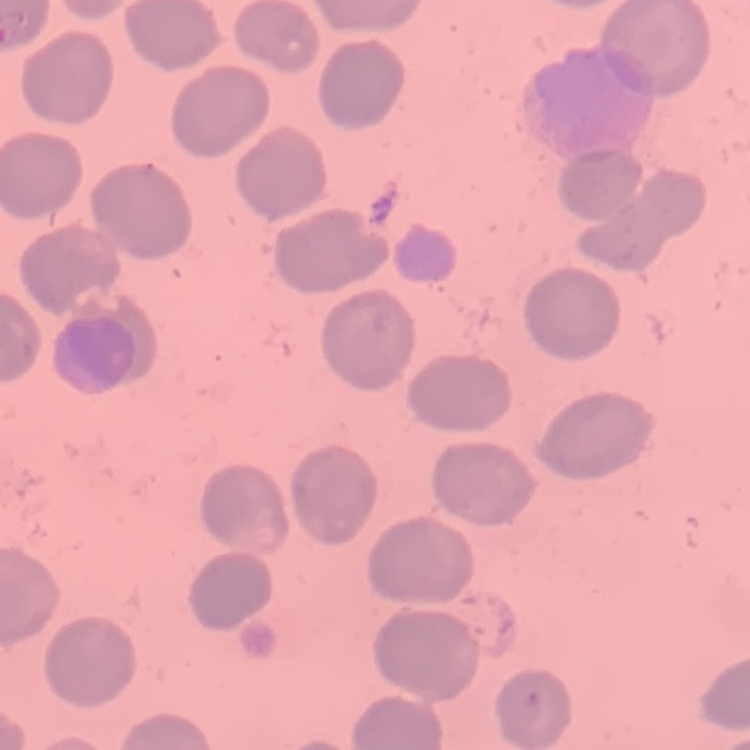

erythrocyte_morphology: no rouleaux formation
preparation: thin blood film
image_type: one tile cut from a larger photomicrograph
stain: Field's or Giemsa